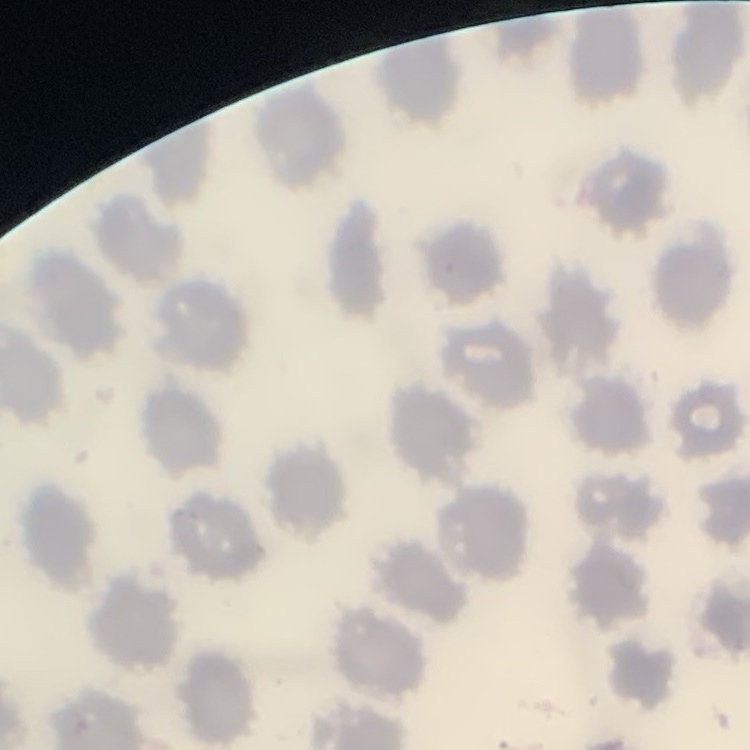

erythrocyte morphology = no rouleaux formation
stain = Field's or Giemsa
image type = one tile cut from a larger photomicrograph
preparation = thin blood smear